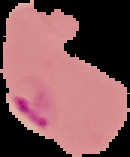 From a thin blood smear. Cell region segmented out of the field of view; the surrounding area is masked to black. Malaria status: parasitized. Image is 130×157 pixels.